Outline each uninfected red blood cell.
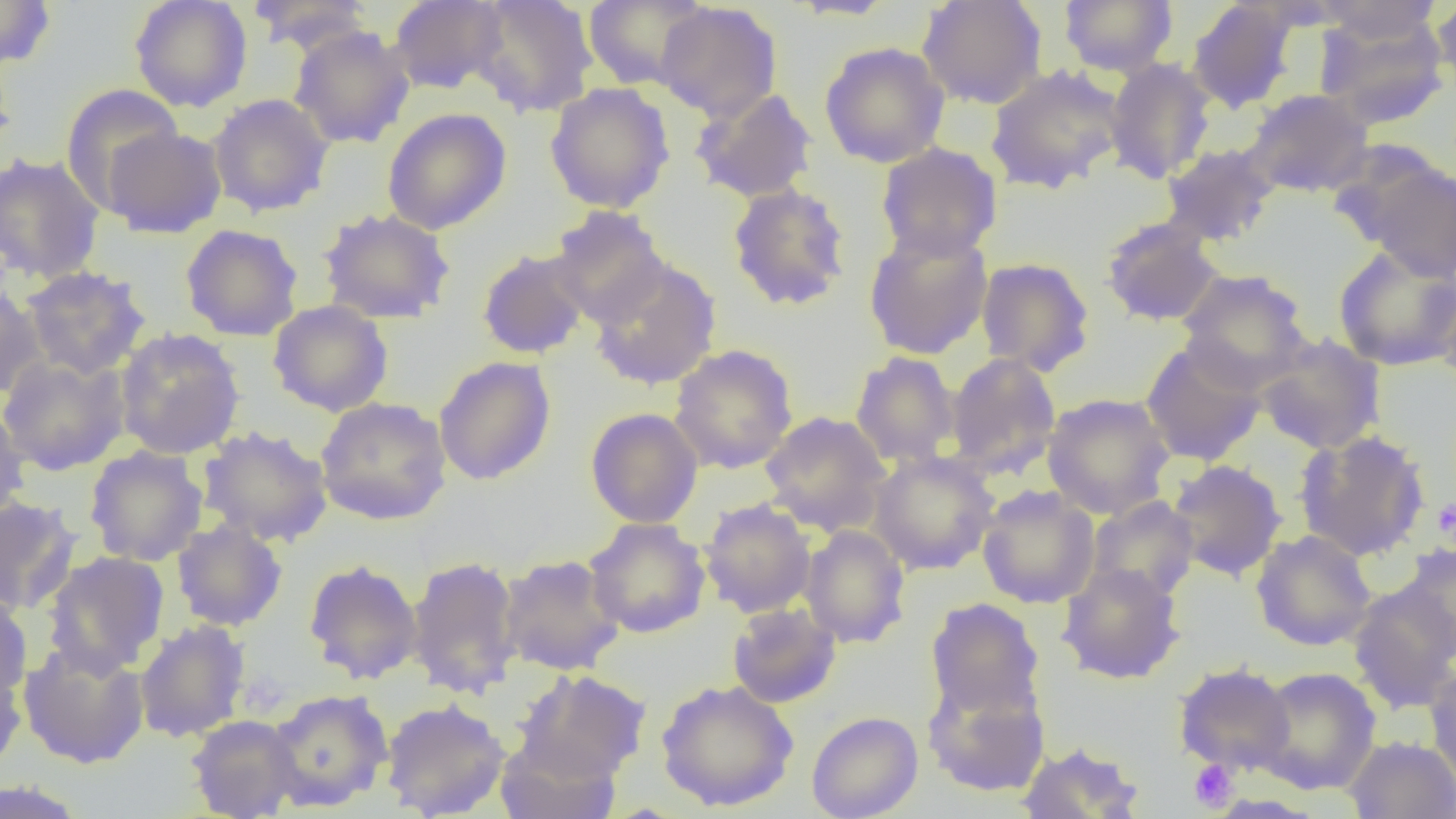
Approximate bounding boxes as (x1, y1, x2, y2) in pixels.
Uninfected red blood cells: (129, 0, 253, 112), (388, 0, 509, 94), (468, 0, 598, 118), (787, 0, 902, 21), (916, 0, 1048, 110), (1059, 0, 1177, 77), (1312, 0, 1444, 43), (1431, 0, 1456, 98), (0, 1, 57, 70), (246, 1, 374, 55), (583, 1, 709, 90), (1186, 1, 1301, 115), (653, 3, 783, 122), (1315, 11, 1450, 129), (289, 25, 415, 149), (819, 41, 950, 168), (0, 44, 17, 174), (1104, 58, 1217, 184), (985, 64, 1126, 194), (544, 82, 675, 213), (60, 84, 185, 209), (690, 88, 818, 203), (1243, 89, 1374, 198), (207, 93, 335, 218), (382, 107, 512, 235), (102, 126, 227, 238), (876, 143, 1003, 261), (1160, 143, 1280, 247), (0, 152, 105, 285), (1354, 157, 1456, 282), (726, 182, 852, 312), (547, 206, 670, 327), (317, 207, 455, 324), (1099, 216, 1224, 327), (180, 223, 304, 342), (863, 225, 994, 360), (1332, 245, 1456, 371), (477, 248, 592, 360), (588, 257, 723, 391), (976, 257, 1095, 376), (20, 266, 152, 380), (1176, 268, 1313, 391), (1434, 270, 1456, 394), (0, 285, 46, 400), (267, 300, 393, 417), (114, 327, 246, 460), (1255, 333, 1386, 456), (1140, 341, 1267, 466), (669, 344, 798, 475), (850, 352, 960, 467), (945, 352, 1062, 478), (0, 355, 130, 475), (433, 356, 556, 485), (1041, 392, 1176, 520), (315, 397, 452, 525), (0, 405, 31, 523), (586, 407, 703, 528), (760, 411, 892, 535), (198, 425, 334, 548), (1294, 430, 1431, 561), (84, 446, 208, 566), (869, 451, 999, 575), (1167, 459, 1288, 582), (977, 485, 1100, 609), (1087, 495, 1199, 602), (0, 496, 83, 616), (699, 497, 816, 618), (585, 517, 710, 638), (171, 520, 288, 632), (799, 525, 910, 649), (1251, 529, 1377, 651), (1397, 543, 1456, 661), (42, 550, 170, 676), (498, 554, 626, 676), (406, 555, 524, 700), (303, 559, 423, 685), (1057, 562, 1185, 685), (1346, 582, 1455, 715), (0, 590, 34, 701), (926, 597, 1045, 719), (727, 602, 841, 709), (134, 619, 251, 742), (18, 641, 150, 769), (0, 655, 28, 776), (1424, 658, 1456, 786), (1174, 662, 1296, 775), (1253, 666, 1381, 795), (514, 669, 650, 782), (922, 672, 1050, 798), (655, 679, 799, 812), (265, 689, 393, 812), (380, 698, 511, 818), (806, 710, 923, 819), (186, 714, 301, 818), (494, 733, 620, 819), (1343, 735, 1456, 818), (1017, 741, 1146, 819), (0, 779, 87, 819).

Platelet locations: (1432, 497, 1456, 544), (1188, 759, 1238, 811). Slide-level diagnosis: negative for blood parasites. 1000x magnification. Thin blood smear. One field of a larger specimen. Light microscopy. Image is 1456×819 pixels.